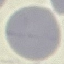
Summary:
  - Malaria status: uninfected
  - Image type: automatically extracted cell patch, resized to 64 × 64 pixels
  - Stain: Giemsa
  - Capture: smartphone camera at the microscope eyepiece
  - Preparation: thin smear